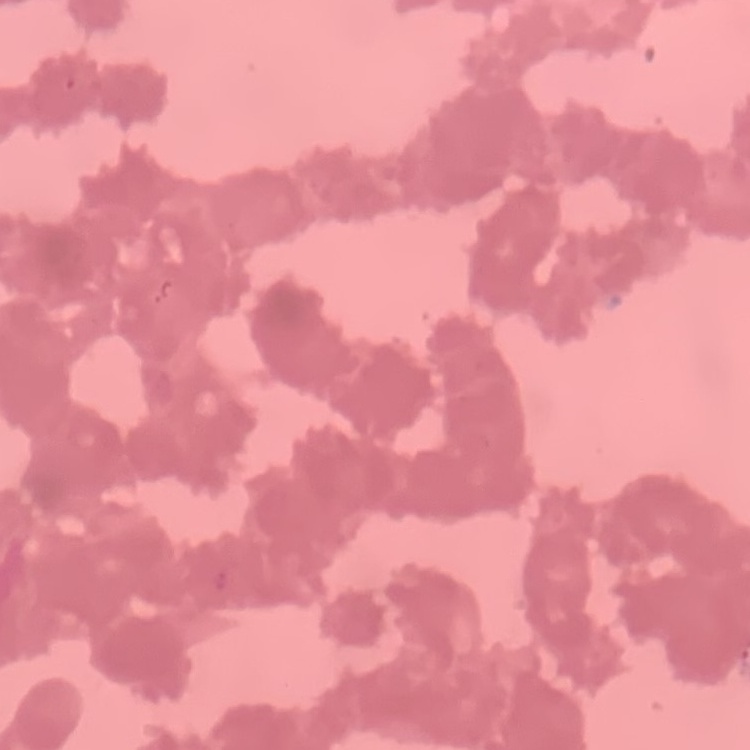

The red blood cells show rouleaux formation. Stained with either Field's or Giemsa. Thin blood smear. Square crop of a larger photomicrograph.